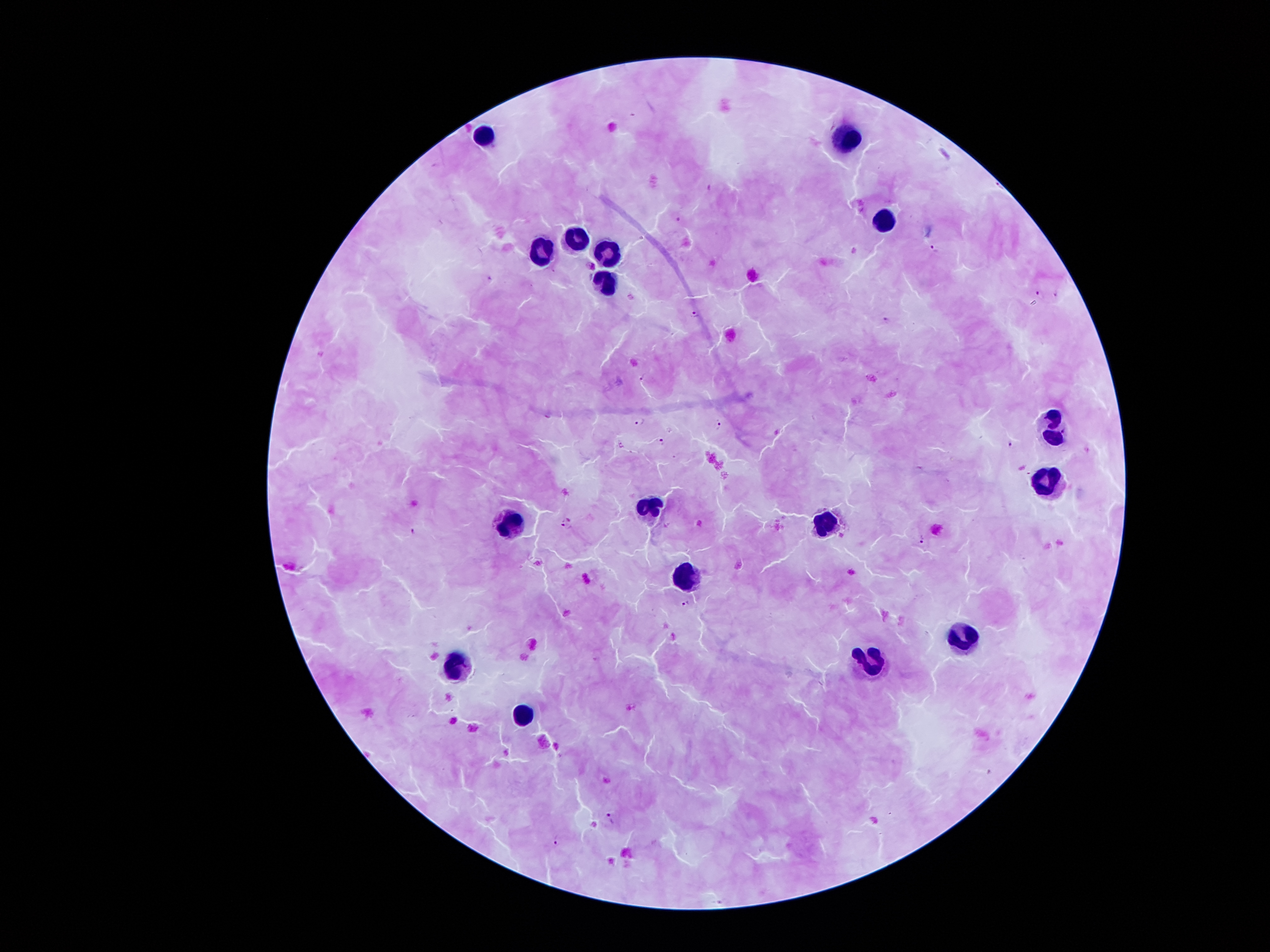
Approximate object centers, in pixels from the top-left corner.
Summary:
  - Leukocyte locations: (x=488, y=137), (x=841, y=140), (x=884, y=219), (x=578, y=232), (x=612, y=243), (x=541, y=247), (x=606, y=281), (x=1053, y=427), (x=1048, y=479), (x=648, y=512), (x=509, y=517), (x=823, y=521), (x=686, y=572), (x=966, y=634), (x=867, y=659), (x=457, y=673), (x=519, y=715)
  - Plasmodium parasite locations: (x=677, y=218), (x=935, y=247), (x=592, y=265), (x=1040, y=293), (x=695, y=314), (x=886, y=320), (x=642, y=376), (x=640, y=423), (x=719, y=425), (x=662, y=441), (x=1011, y=444), (x=568, y=524), (x=412, y=530), (x=923, y=540), (x=538, y=563), (x=685, y=605), (x=611, y=819), (x=557, y=840)
  - Image size: 1270×952 pixels
  - Field of view: one from this slide
  - Magnification: 100x
  - Capture: smartphone camera through the microscope eyepiece
  - Stain: Giemsa
  - Patient malaria status: infected with Plasmodium falciparum
  - Preparation: thick blood smear